Classify this cell by malaria status.
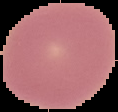

It is uninfected.

{
  "image_size": "118×112 pixels",
  "image_type": "segmented cell region with the area outside set to black",
  "preparation": "thin blood film"
}